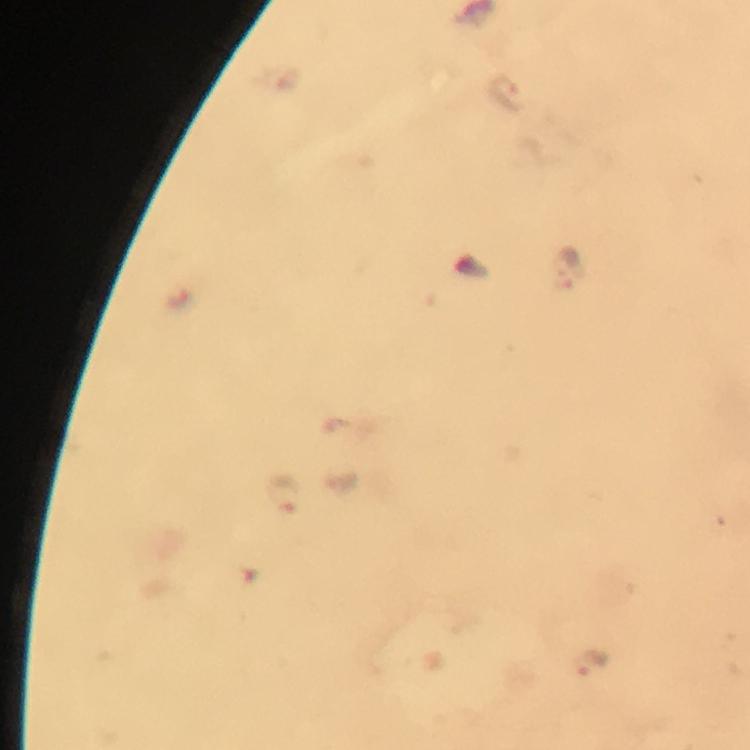

cropped from = one field of view
capture = smartphone mounted on the microscope
stain = Giemsa
context = from a diagnostic examination for malaria
preparation = thick blood smear
malaria parasite locations = approximate object centers, in pixels from the top-left corner: (x=506, y=95), (x=278, y=492), (x=590, y=663)
image size = 750×750 pixels
magnification = 100x
immersion oil = applied